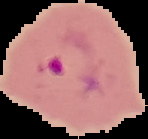 From a thin blood smear. Image is 148×139 pixels. The area outside the segmented cell region is set to black. Result: malaria parasites identified.